Classify this cell by malaria status.
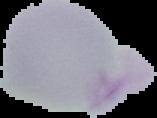

Uninfected.

From a thin blood film. Image is 157×118 pixels. The area outside the segmented cell region is set to black.